Outline each blood parasite and name the species.
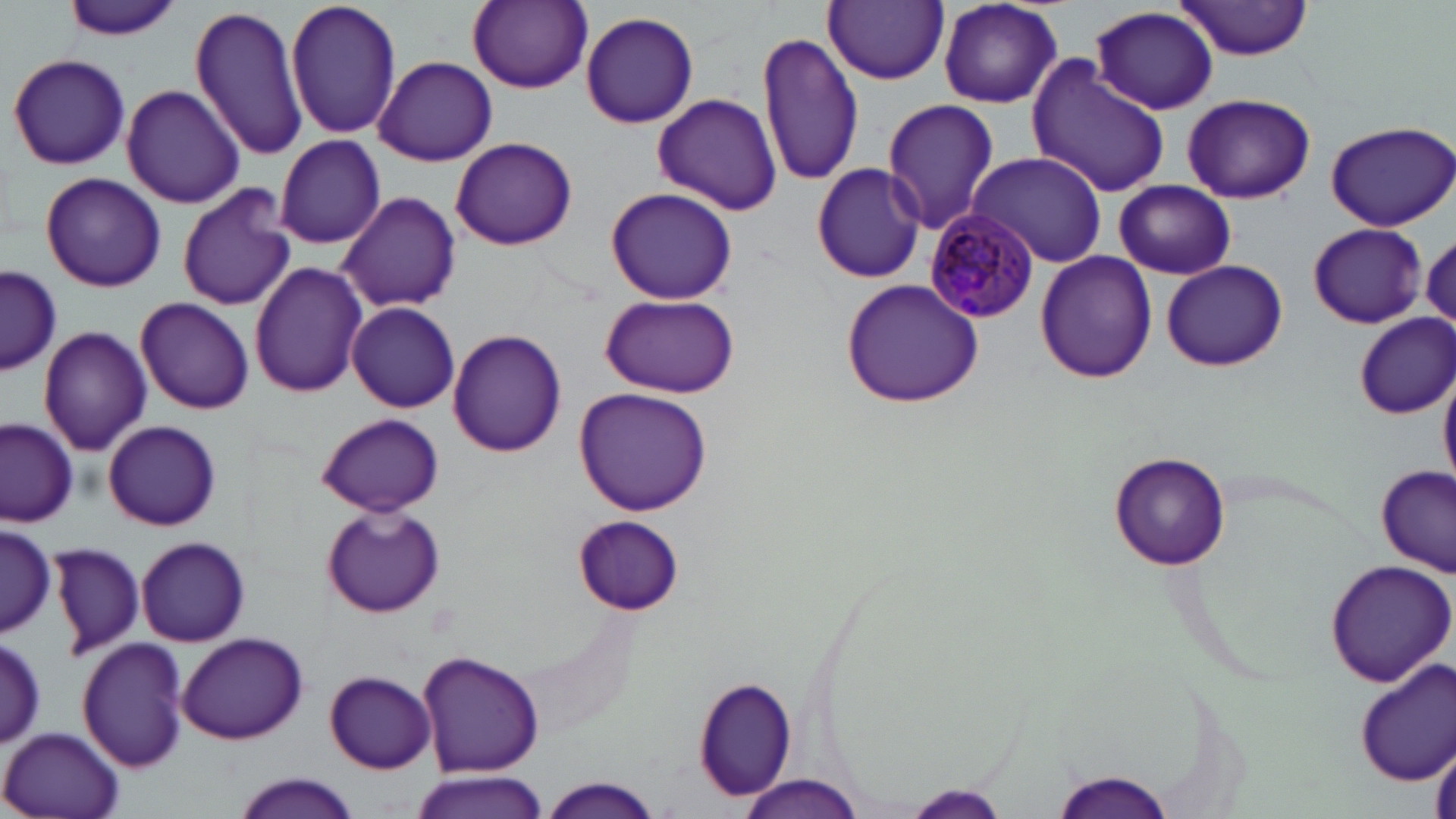

Approximate bounding boxes as (x1,y1)-(x2,y2) corner pairs in pixels.
Plasmodium malariae-infected red blood cells: (922,211)-(1041,324).
No Plasmodium falciparum, Plasmodium ovale, Plasmodium vivax, Babesia divergens, or Trypanosoma brucei observed.

Uninfected red blood cell locations: (59,0)-(182,44), (285,0)-(400,142), (467,0)-(592,91), (823,1)-(949,85), (1174,1)-(1319,61), (936,2)-(1067,108), (189,6)-(309,161), (1090,6)-(1219,116), (580,10)-(699,130), (757,29)-(864,190), (6,53)-(130,171), (374,55)-(497,166), (1028,60)-(1172,199), (121,85)-(244,208), (651,93)-(781,215), (1182,93)-(1314,203), (881,98)-(999,234), (1325,121)-(1456,232), (450,136)-(577,250), (274,137)-(389,250), (968,151)-(1105,266), (810,163)-(926,284), (40,171)-(166,293), (1114,180)-(1236,279), (177,184)-(296,312), (605,187)-(738,305), (338,190)-(461,314), (1308,222)-(1429,328), (1035,251)-(1158,382), (1162,259)-(1288,372), (248,261)-(369,399), (2,266)-(60,376), (841,279)-(986,408), (599,292)-(738,399), (134,298)-(255,415), (347,303)-(460,413), (1354,314)-(1455,418), (39,325)-(152,457), (448,330)-(567,456), (1438,368)-(1456,489), (575,388)-(713,516), (318,414)-(444,516), (0,417)-(80,525), (103,420)-(222,530), (1110,452)-(1231,570), (1376,466)-(1455,576), (321,503)-(446,619), (572,515)-(683,614), (1,518)-(57,638), (135,537)-(250,647), (48,540)-(144,661), (1323,557)-(1456,688), (177,632)-(308,744), (1,634)-(44,747), (77,637)-(190,773), (419,652)-(545,776), (1355,658)-(1456,785), (326,671)-(435,771), (695,676)-(798,801), (0,725)-(127,819), (1429,740)-(1456,819), (1051,770)-(1177,818), (412,771)-(550,819), (232,772)-(362,819), (737,775)-(864,817), (537,776)-(664,819), (903,785)-(1010,818). Slide-level diagnosis: Plasmodium malariae. Thin blood film. One field of a larger specimen. 1000x magnification. Optical microscopy. May-Grünwald-Giemsa-stained preparation. Image is 1456×819 pixels.